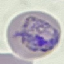

Malaria status: parasitized. Thin blood film. Giemsa stain. Cell patch, automatically extracted from a larger field of view and resized to 64 × 64 pixels. Photographed with a smartphone camera at the microscope eyepiece.